Identify the blood parasite species.
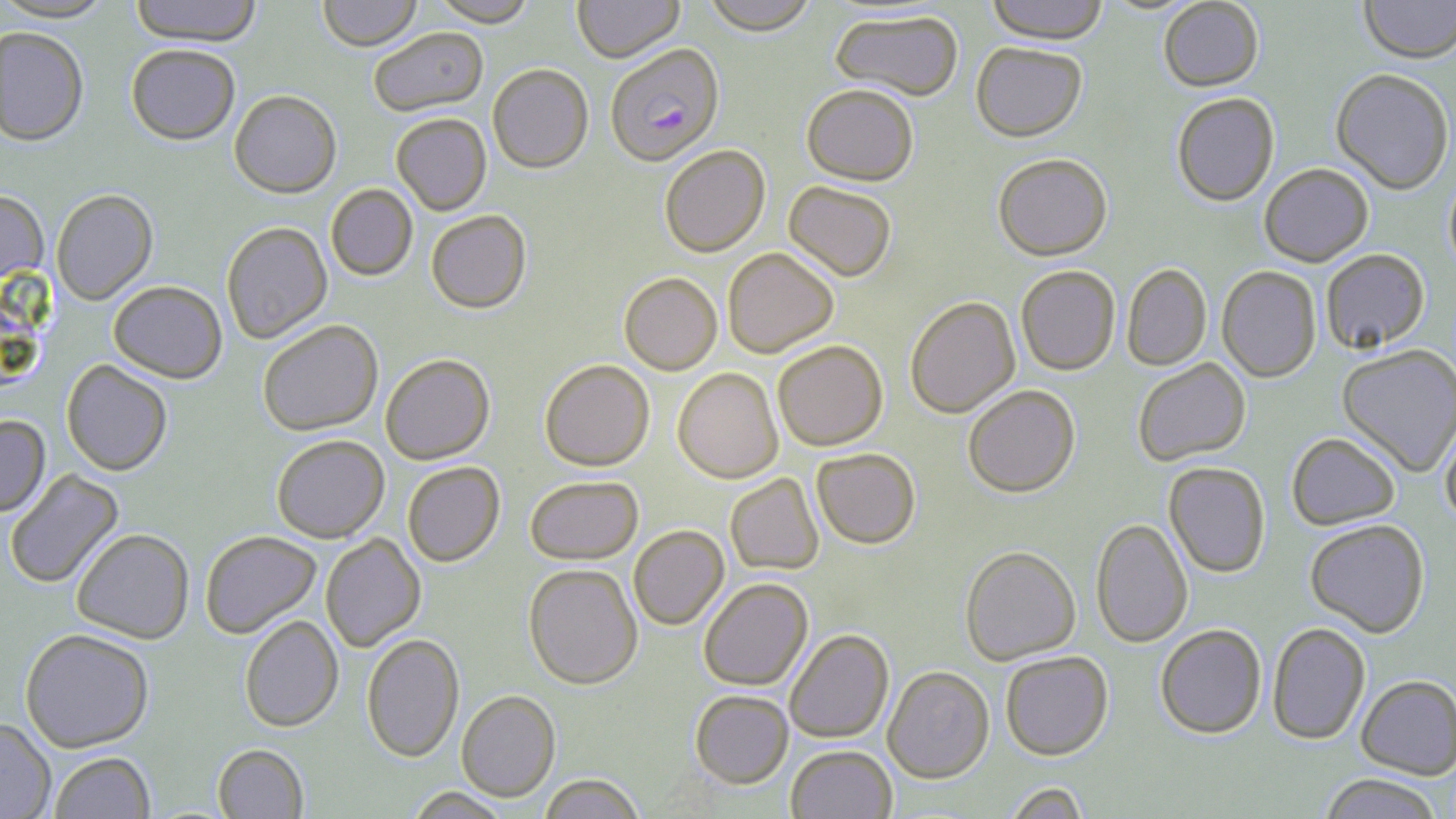
Plasmodium falciparum.

Approximate bounding boxes as (x1, y1, x2, y2) in pixels. Uninfected red blood cell locations: (0, 0, 116, 22), (129, 0, 263, 45), (317, 0, 422, 51), (429, 0, 539, 26), (573, 0, 684, 63), (701, 0, 820, 35), (986, 0, 1109, 46), (1158, 0, 1264, 93), (1359, 0, 1456, 66), (830, 9, 963, 103), (0, 26, 89, 146), (368, 26, 488, 116), (126, 43, 240, 145), (971, 43, 1087, 144), (487, 63, 593, 173), (1330, 70, 1454, 196), (802, 84, 918, 186), (229, 89, 342, 197), (1172, 94, 1280, 207), (391, 112, 492, 215), (659, 144, 771, 257), (993, 155, 1112, 262), (1260, 165, 1373, 268), (1444, 170, 1456, 281), (783, 181, 897, 282), (325, 184, 417, 281), (51, 188, 158, 304), (0, 189, 48, 283), (425, 209, 532, 313), (221, 221, 332, 344), (722, 247, 839, 358), (1321, 249, 1430, 355), (1122, 264, 1212, 371), (1015, 266, 1120, 376), (1217, 267, 1321, 383), (619, 272, 722, 375), (108, 280, 227, 383), (905, 297, 1021, 418), (257, 319, 383, 435), (773, 340, 888, 451), (1337, 345, 1456, 477), (380, 353, 495, 465), (61, 359, 173, 475), (539, 359, 654, 471), (1133, 359, 1250, 467), (672, 368, 783, 483), (963, 385, 1080, 498), (0, 415, 50, 516), (1440, 419, 1456, 528), (1287, 433, 1400, 531), (271, 434, 390, 542), (811, 448, 920, 550), (402, 461, 505, 566), (1164, 463, 1271, 579), (4, 469, 124, 589), (725, 473, 824, 575), (525, 475, 643, 564), (1090, 519, 1193, 648), (1305, 521, 1430, 638), (628, 525, 729, 630), (71, 528, 194, 643), (200, 530, 321, 638), (320, 534, 426, 651), (960, 545, 1081, 666), (524, 563, 643, 689), (699, 578, 813, 691), (240, 615, 343, 732), (1267, 623, 1370, 745), (1155, 625, 1266, 740), (19, 628, 155, 752), (784, 629, 894, 744), (361, 633, 464, 762), (1000, 651, 1113, 761), (883, 666, 994, 783), (1356, 675, 1456, 780), (456, 690, 560, 801), (690, 690, 793, 789), (0, 718, 56, 819), (212, 743, 309, 818), (786, 745, 897, 819), (49, 752, 155, 818), (538, 774, 645, 819), (1320, 774, 1444, 819), (1003, 781, 1090, 819), (404, 787, 512, 818). Plasmodium falciparum-infected red blood cell locations: (605, 43, 724, 167). Image is 1456×819 pixels. Optical microscopy. Thin blood film. Captured at 1000x magnification. May-Grünwald-Giemsa stain. One field of a larger specimen.